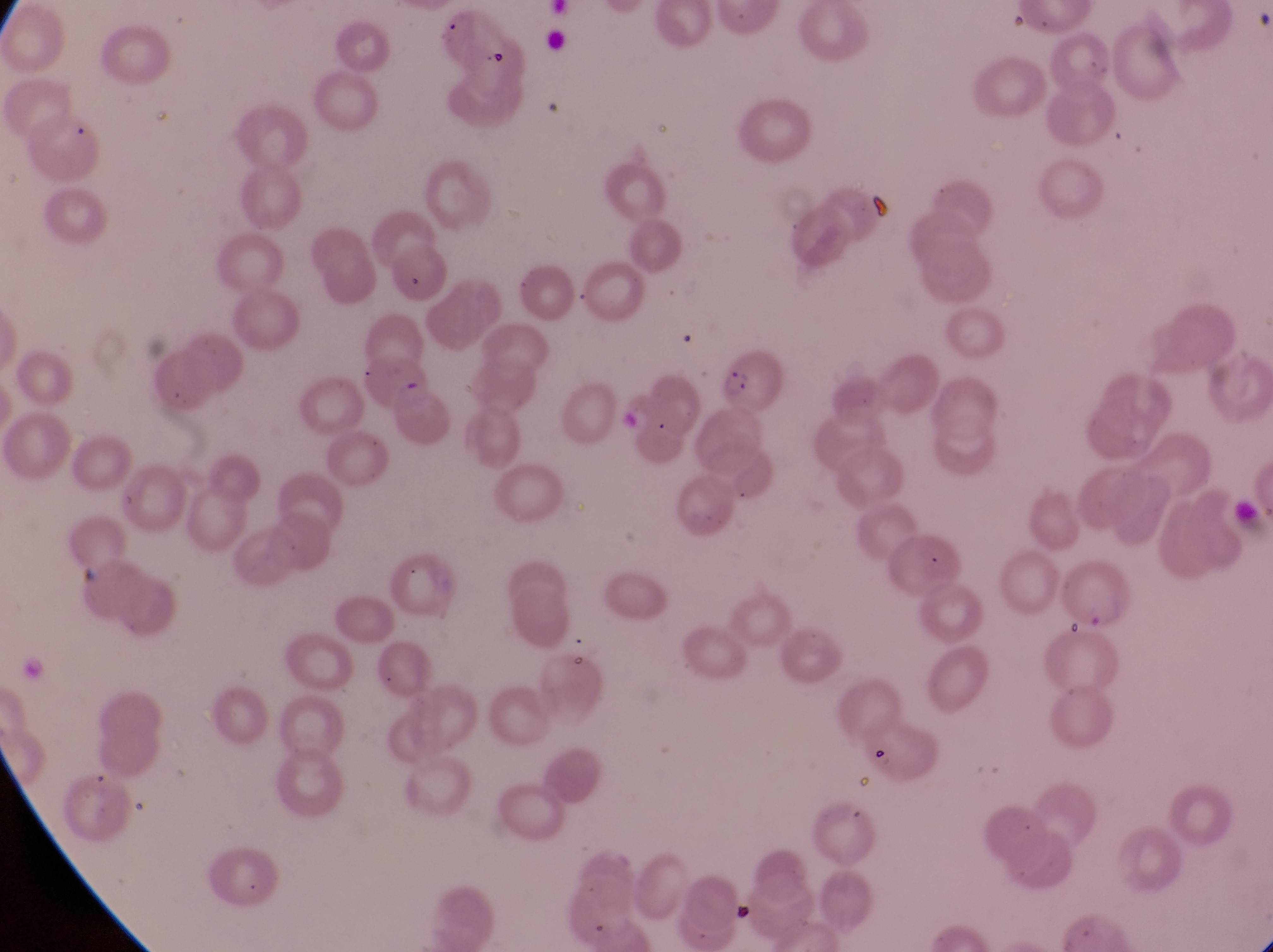

capture = smartphone photograph through the eyepiece of an Olympus CX-23 microscope
country = Uganda
magnification = 1000x
image size = 1273×952 pixels
field of view = single
artifact (platelet-like body, stain precipitate, or debris) locations = approximate bounding boxes as (left, top, right, bottom) in pixels: (868, 183, 900, 218)
parasitised red blood cell locations = approximate bounding boxes as (left, top, right, bottom) in pixels: (712, 355, 781, 417)
preparation = thin blood smear